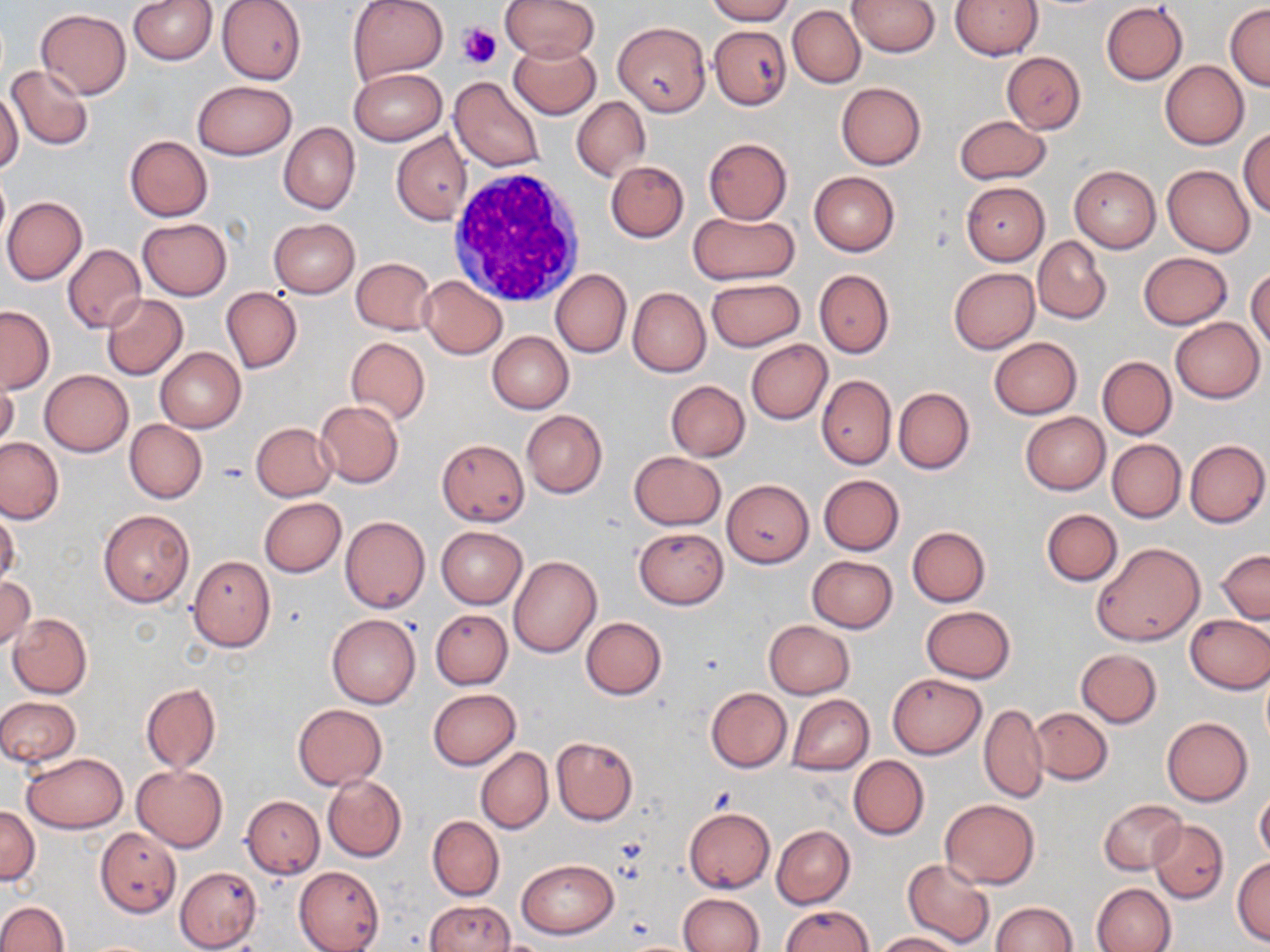

Summary:
  - Coordinate format: approximate bounding boxes as named x1/y1/x2/y2 corners in pixels
  - White blood cell locations: (x1=448, y1=166, x2=587, y2=310)
  - Uninfected red blood cell locations: (x1=130, y1=0, x2=217, y2=65), (x1=217, y1=0, x2=307, y2=84), (x1=347, y1=0, x2=449, y2=84), (x1=499, y1=0, x2=600, y2=62), (x1=706, y1=0, x2=794, y2=24), (x1=848, y1=0, x2=940, y2=56), (x1=950, y1=0, x2=1042, y2=60), (x1=1101, y1=3, x2=1187, y2=85), (x1=1225, y1=4, x2=1270, y2=90), (x1=786, y1=5, x2=935, y2=69), (x1=789, y1=5, x2=864, y2=88), (x1=36, y1=8, x2=131, y2=98), (x1=614, y1=20, x2=711, y2=116), (x1=710, y1=24, x2=790, y2=110), (x1=508, y1=43, x2=602, y2=119), (x1=1002, y1=51, x2=1086, y2=134), (x1=1160, y1=61, x2=1248, y2=149), (x1=7, y1=64, x2=94, y2=150), (x1=350, y1=69, x2=446, y2=145), (x1=449, y1=77, x2=545, y2=172), (x1=192, y1=80, x2=297, y2=160), (x1=835, y1=82, x2=925, y2=170), (x1=0, y1=90, x2=23, y2=175), (x1=572, y1=97, x2=649, y2=180), (x1=954, y1=115, x2=1051, y2=185), (x1=279, y1=122, x2=359, y2=215), (x1=1239, y1=128, x2=1270, y2=216), (x1=391, y1=132, x2=470, y2=225), (x1=124, y1=136, x2=212, y2=221), (x1=704, y1=138, x2=792, y2=224), (x1=605, y1=160, x2=689, y2=242), (x1=1163, y1=164, x2=1255, y2=257), (x1=1069, y1=165, x2=1160, y2=252), (x1=0, y1=170, x2=10, y2=247), (x1=809, y1=172, x2=899, y2=256), (x1=961, y1=182, x2=1049, y2=264), (x1=2, y1=196, x2=87, y2=284), (x1=688, y1=211, x2=798, y2=286), (x1=138, y1=218, x2=233, y2=300), (x1=269, y1=218, x2=360, y2=297), (x1=1033, y1=235, x2=1112, y2=324), (x1=61, y1=244, x2=147, y2=334), (x1=1138, y1=252, x2=1233, y2=329), (x1=351, y1=257, x2=435, y2=334), (x1=948, y1=268, x2=1039, y2=353), (x1=1247, y1=268, x2=1270, y2=350), (x1=550, y1=269, x2=631, y2=358), (x1=813, y1=269, x2=893, y2=358), (x1=420, y1=276, x2=507, y2=358), (x1=707, y1=277, x2=805, y2=352), (x1=221, y1=288, x2=302, y2=373), (x1=628, y1=288, x2=711, y2=377), (x1=101, y1=294, x2=188, y2=380), (x1=0, y1=305, x2=54, y2=393), (x1=1170, y1=317, x2=1264, y2=403), (x1=487, y1=331, x2=573, y2=413), (x1=345, y1=337, x2=430, y2=424), (x1=990, y1=337, x2=1082, y2=419), (x1=746, y1=340, x2=832, y2=425), (x1=155, y1=346, x2=246, y2=432), (x1=1097, y1=356, x2=1177, y2=439), (x1=1, y1=370, x2=20, y2=454), (x1=39, y1=370, x2=133, y2=456), (x1=816, y1=374, x2=897, y2=468), (x1=666, y1=380, x2=750, y2=461), (x1=894, y1=387, x2=975, y2=474), (x1=315, y1=400, x2=404, y2=487), (x1=521, y1=409, x2=608, y2=498), (x1=1020, y1=412, x2=1110, y2=495), (x1=124, y1=420, x2=206, y2=504), (x1=250, y1=423, x2=337, y2=500), (x1=0, y1=436, x2=66, y2=525), (x1=436, y1=438, x2=529, y2=525), (x1=1107, y1=439, x2=1185, y2=521), (x1=1184, y1=439, x2=1269, y2=527), (x1=629, y1=451, x2=725, y2=529), (x1=818, y1=474, x2=904, y2=555), (x1=722, y1=480, x2=813, y2=568), (x1=260, y1=497, x2=347, y2=577), (x1=99, y1=509, x2=194, y2=608), (x1=1041, y1=509, x2=1122, y2=585), (x1=0, y1=511, x2=21, y2=588), (x1=340, y1=517, x2=430, y2=613), (x1=436, y1=526, x2=527, y2=608), (x1=907, y1=526, x2=990, y2=606), (x1=634, y1=527, x2=729, y2=609), (x1=1091, y1=542, x2=1205, y2=646), (x1=1217, y1=549, x2=1270, y2=623), (x1=509, y1=555, x2=601, y2=657), (x1=187, y1=556, x2=275, y2=650), (x1=806, y1=556, x2=898, y2=632), (x1=0, y1=576, x2=35, y2=652), (x1=921, y1=606, x2=1016, y2=683), (x1=431, y1=610, x2=512, y2=689), (x1=8, y1=613, x2=92, y2=698), (x1=1185, y1=613, x2=1270, y2=694), (x1=327, y1=614, x2=421, y2=709), (x1=581, y1=617, x2=666, y2=699), (x1=763, y1=620, x2=855, y2=699), (x1=1075, y1=648, x2=1162, y2=727), (x1=888, y1=673, x2=986, y2=758), (x1=141, y1=683, x2=220, y2=772), (x1=706, y1=688, x2=792, y2=771), (x1=428, y1=689, x2=520, y2=769), (x1=787, y1=694, x2=872, y2=776), (x1=0, y1=696, x2=81, y2=767), (x1=293, y1=703, x2=387, y2=790), (x1=979, y1=703, x2=1048, y2=803), (x1=1030, y1=707, x2=1112, y2=785), (x1=1162, y1=717, x2=1253, y2=806), (x1=551, y1=736, x2=638, y2=825), (x1=476, y1=747, x2=553, y2=834), (x1=21, y1=752, x2=127, y2=833), (x1=848, y1=755, x2=929, y2=840), (x1=132, y1=764, x2=227, y2=851), (x1=322, y1=774, x2=407, y2=863), (x1=1255, y1=788, x2=1270, y2=865), (x1=242, y1=795, x2=324, y2=878), (x1=940, y1=799, x2=1039, y2=888), (x1=1099, y1=799, x2=1187, y2=875), (x1=1, y1=806, x2=40, y2=884), (x1=683, y1=808, x2=775, y2=892), (x1=427, y1=815, x2=504, y2=900), (x1=1149, y1=820, x2=1228, y2=902), (x1=772, y1=826, x2=855, y2=908), (x1=95, y1=828, x2=181, y2=917), (x1=1232, y1=857, x2=1270, y2=945), (x1=518, y1=858, x2=617, y2=938), (x1=903, y1=858, x2=995, y2=948), (x1=294, y1=865, x2=385, y2=952), (x1=175, y1=867, x2=262, y2=950), (x1=1090, y1=883, x2=1175, y2=952), (x1=677, y1=893, x2=764, y2=952), (x1=426, y1=900, x2=514, y2=951), (x1=0, y1=901, x2=69, y2=952), (x1=990, y1=902, x2=1078, y2=952), (x1=781, y1=904, x2=871, y2=952), (x1=874, y1=932, x2=963, y2=951)
  - Platelet locations: (x1=458, y1=23, x2=501, y2=68)
  - Slide-level diagnosis: negative for blood parasites
  - Magnification: 1000x
  - Preparation: thin blood film
  - Modality: optical microscopy
  - Field of view: one of a larger specimen
  - Image size: 1270×952 pixels
  - Stain: May-Grünwald-Giemsa